Locate Plasmodium parasites and leukocytes.
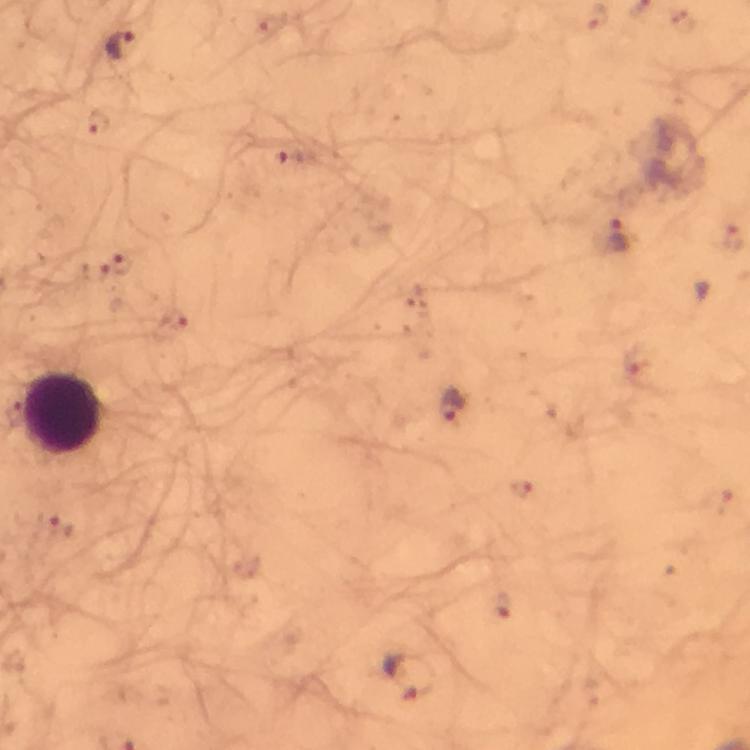

Approximate centers as (x, y) in pixels.
Plasmodium parasites: (121, 46), (97, 121), (290, 157), (618, 236), (732, 236), (122, 263), (177, 320), (452, 404), (520, 489), (57, 526), (500, 604), (408, 675).
Leukocytes: (64, 411).

{
  "immersion_oil": "used",
  "cropped_from": "one field of view",
  "image_size": "750×750 pixels",
  "magnification": "100x",
  "stain": "Giemsa",
  "context": "from a malaria diagnostic workup",
  "preparation": "thick blood film",
  "capture": "smartphone photograph through a microscope"
}